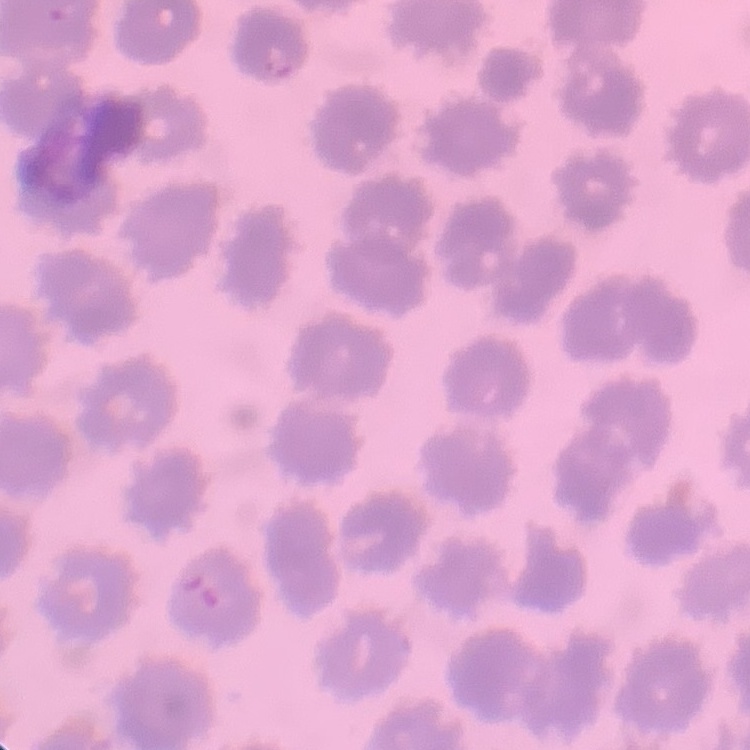
erythrocyte morphology = no rouleaux formation
preparation = thin blood smear
stain = Field's or Giemsa
image type = one tile cut from a larger photomicrograph